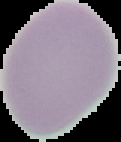

result = no malaria parasites seen
preparation = thin blood film
image type = cell region segmented out of the field of view; surrounding area masked to black
image size = 121×142 pixels